Outline each blood parasite and name the species.
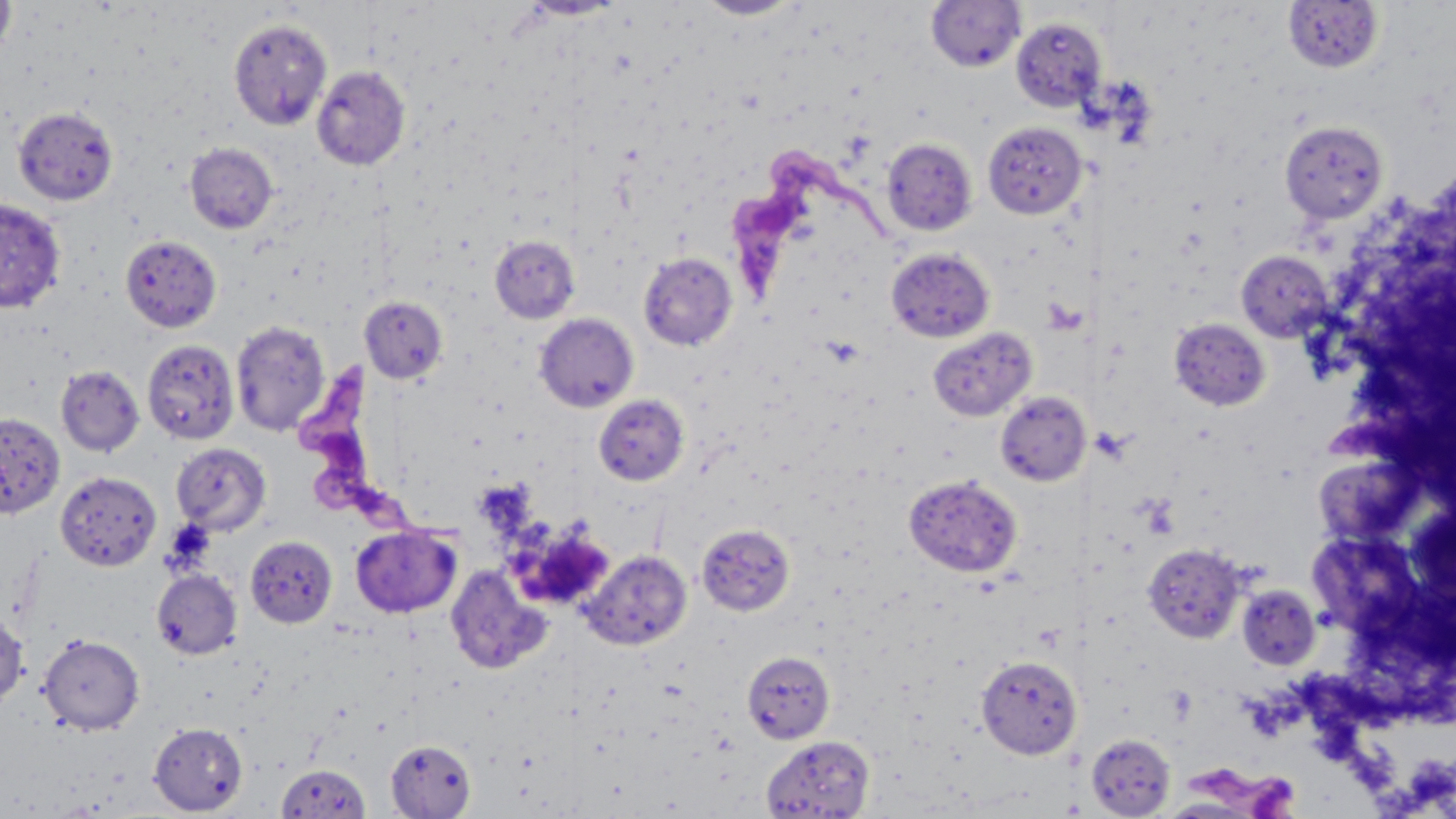

Approximate bounding boxes as [x1, y1, x2, y2] in pixels.
Trypanosoma brucei: [733, 145, 901, 300], [302, 369, 467, 546], [1186, 758, 1312, 819].
No Plasmodium falciparum, Plasmodium ovale, Plasmodium malariae, Plasmodium vivax, or Babesia divergens observed.

Summary:
  - Uninfected red blood cell locations: [0, 0, 16, 64], [695, 0, 804, 20], [926, 0, 1025, 72], [1283, 1, 1384, 73], [1010, 18, 1106, 112], [229, 19, 332, 130], [312, 65, 411, 170], [13, 106, 118, 205], [982, 121, 1086, 219], [1280, 121, 1389, 223], [881, 138, 977, 236], [185, 142, 278, 234], [0, 197, 66, 312], [120, 235, 222, 332], [489, 235, 580, 323], [886, 248, 994, 342], [1236, 251, 1332, 341], [638, 252, 737, 350], [359, 296, 448, 384], [534, 313, 639, 413], [1170, 319, 1270, 411], [230, 320, 330, 436], [927, 327, 1036, 421], [142, 339, 239, 444], [56, 365, 144, 457], [995, 391, 1091, 486], [594, 395, 689, 486], [0, 411, 65, 519], [171, 443, 271, 535], [54, 471, 161, 571], [903, 474, 1023, 578], [697, 524, 795, 616], [350, 525, 461, 618], [246, 536, 337, 628], [1142, 543, 1246, 642], [580, 550, 692, 650], [445, 563, 553, 675], [151, 569, 242, 660], [1238, 585, 1321, 669], [0, 611, 29, 708], [38, 634, 144, 735], [741, 650, 835, 744], [975, 654, 1082, 759], [149, 722, 248, 815], [1085, 733, 1178, 817], [761, 735, 875, 818], [386, 739, 476, 818], [276, 763, 371, 817]
  - Platelet locations: [506, 520, 615, 611]
  - Slide-level diagnosis: Trypanosoma brucei
  - Preparation: thin blood film
  - Magnification: 1000x
  - Stain: May-Grünwald-Giemsa
  - Field of view: single
  - Image size: 1456×819 pixels
  - Modality: optical microscopy